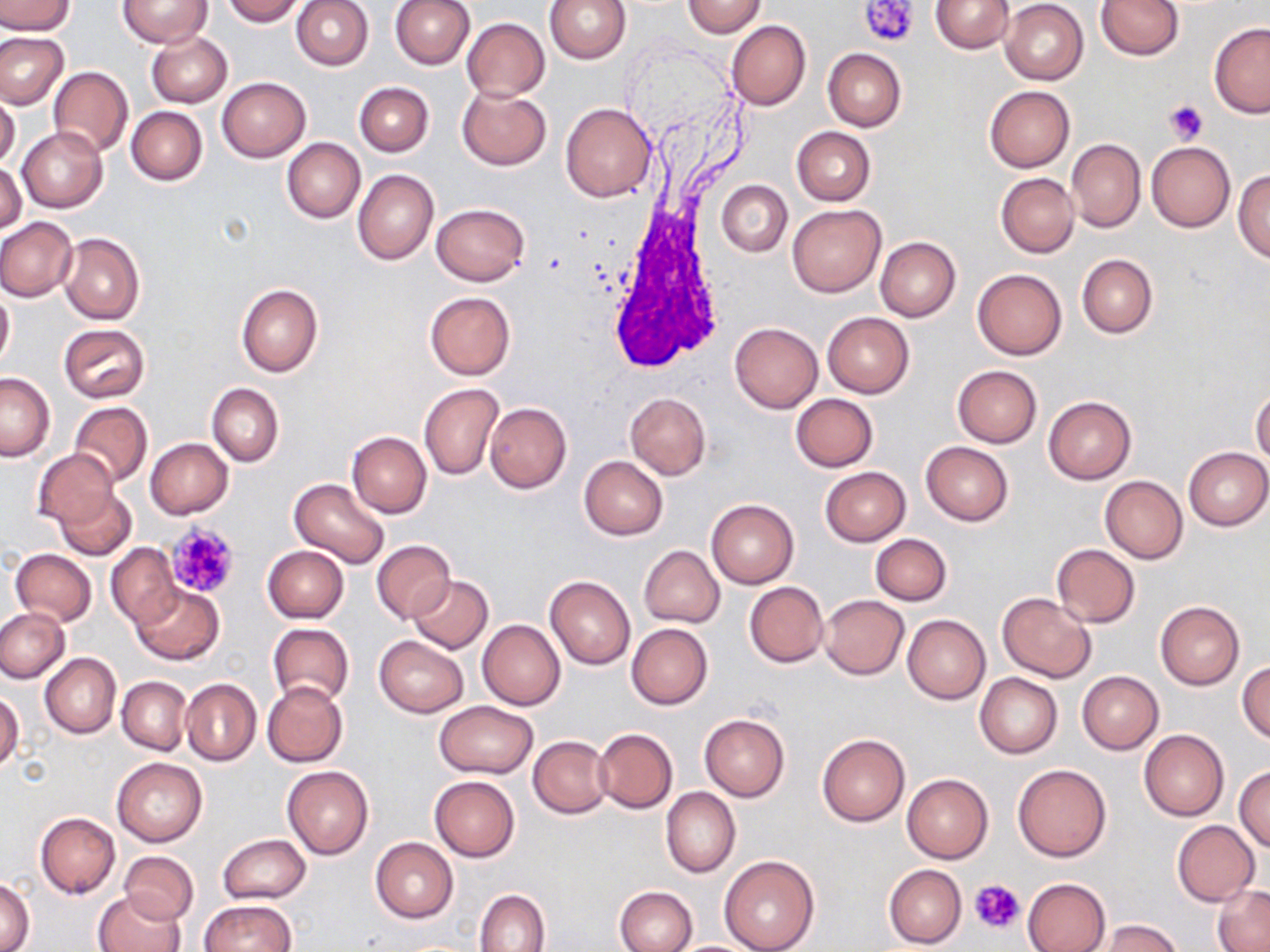
Approximate bounding boxes as [x1, y1, x2, y2] in pixels. Platelet locations: [861, 0, 920, 48], [1164, 100, 1207, 144], [165, 521, 241, 601], [970, 878, 1024, 934]. Uninfected red blood cell locations: [0, 0, 75, 36], [118, 0, 213, 48], [221, 0, 304, 25], [291, 0, 373, 71], [390, 0, 475, 68], [545, 0, 631, 64], [683, 0, 766, 38], [931, 0, 1014, 54], [1000, 1, 1088, 85], [1096, 1, 1184, 60], [461, 18, 549, 100], [725, 20, 810, 111], [1209, 22, 1270, 118], [0, 31, 70, 109], [147, 32, 232, 107], [822, 48, 906, 131], [49, 67, 134, 158], [217, 77, 310, 162], [353, 82, 433, 156], [984, 85, 1075, 172], [456, 86, 552, 169], [0, 92, 20, 170], [559, 103, 657, 202], [126, 106, 207, 185], [791, 126, 876, 206], [17, 127, 107, 213], [282, 138, 365, 222], [1066, 139, 1145, 232], [1146, 142, 1236, 232], [1, 162, 26, 237], [1235, 168, 1270, 263], [353, 170, 439, 265], [995, 173, 1078, 258], [717, 180, 792, 256], [432, 203, 529, 286], [787, 206, 884, 296], [0, 217, 77, 301], [58, 232, 145, 324], [874, 237, 960, 322], [1076, 253, 1157, 339], [973, 268, 1067, 359], [237, 284, 323, 378], [0, 287, 14, 372], [424, 291, 516, 380], [821, 311, 915, 398], [730, 322, 823, 413], [57, 323, 149, 402], [951, 366, 1042, 448], [0, 372, 55, 461], [207, 383, 283, 466], [419, 383, 502, 480], [1252, 389, 1270, 468], [625, 393, 711, 479], [790, 393, 878, 472], [1043, 396, 1137, 484], [69, 401, 153, 486], [485, 402, 571, 493], [346, 431, 432, 517], [145, 438, 232, 519], [920, 441, 1014, 526], [1184, 446, 1270, 531], [33, 448, 118, 531], [579, 456, 668, 540], [819, 466, 911, 545], [1100, 476, 1188, 563], [289, 477, 390, 568], [54, 485, 137, 561], [706, 498, 799, 589], [870, 534, 952, 605], [371, 540, 456, 624], [106, 542, 182, 628], [1051, 543, 1140, 628], [263, 545, 349, 622], [640, 545, 725, 628], [9, 548, 96, 627], [407, 575, 492, 653], [545, 575, 635, 670], [131, 582, 223, 664], [744, 582, 830, 667], [996, 593, 1097, 682], [819, 595, 908, 680], [1155, 600, 1245, 690], [0, 607, 71, 682], [902, 614, 990, 704], [477, 620, 565, 709], [268, 623, 355, 708], [627, 623, 713, 709], [374, 635, 469, 717], [40, 653, 121, 738], [1237, 660, 1270, 743], [1076, 670, 1163, 754], [975, 673, 1062, 758], [117, 676, 191, 755], [181, 678, 261, 765], [263, 681, 348, 768], [0, 691, 25, 773], [433, 701, 539, 778], [699, 714, 790, 801], [594, 728, 678, 813], [1138, 729, 1229, 821], [817, 733, 909, 826], [529, 736, 611, 818], [112, 756, 207, 848], [1012, 763, 1113, 862], [1234, 765, 1270, 852], [281, 766, 373, 859], [901, 774, 994, 863], [429, 777, 520, 862], [662, 787, 740, 878], [35, 812, 120, 898], [1171, 819, 1259, 905], [218, 834, 310, 904], [370, 837, 458, 923], [118, 851, 199, 925], [718, 856, 820, 952], [883, 865, 966, 948], [0, 876, 34, 952], [1022, 877, 1111, 952], [1213, 885, 1270, 951], [615, 886, 697, 952], [94, 889, 186, 952], [475, 889, 550, 952], [200, 900, 297, 951], [1096, 919, 1183, 952]. White blood cell locations: [603, 196, 732, 380]. Slide-level diagnosis: no evidence of blood parasites. Image is 1270×952 pixels. Optical microscopy. Captured at 1000x magnification. Thin blood smear. May-Grünwald-Giemsa stain. One field of a larger specimen.